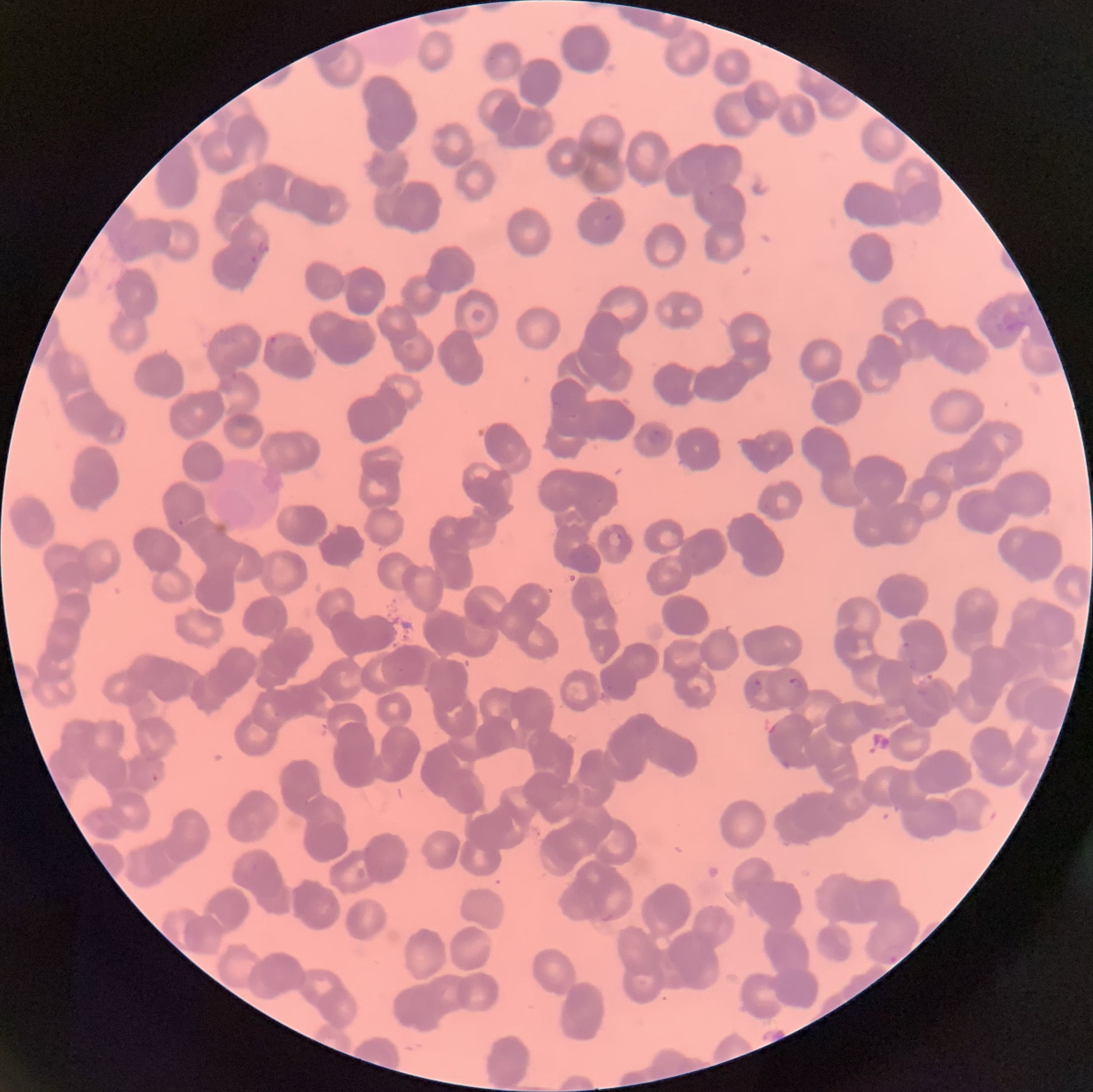
Summary:
  - Coordinate format: approximate bounding boxes as named x1/y1/x2/y2 corners in pixels
  - Plasmodium parasite locations: (x1=707, y1=190, x2=715, y2=196), (x1=604, y1=214, x2=615, y2=221), (x1=257, y1=237, x2=271, y2=254), (x1=250, y1=255, x2=259, y2=263), (x1=266, y1=335, x2=278, y2=347), (x1=552, y1=400, x2=562, y2=412), (x1=647, y1=429, x2=665, y2=444), (x1=607, y1=530, x2=623, y2=547), (x1=903, y1=641, x2=912, y2=649), (x1=909, y1=659, x2=917, y2=672), (x1=789, y1=676, x2=803, y2=689), (x1=754, y1=678, x2=762, y2=693), (x1=979, y1=795, x2=998, y2=831), (x1=882, y1=944, x2=901, y2=963)
  - Plasmodium parasites too small for a box (approximate object centers, named x/y in pixels): (x=181, y=522)
  - Preparation: thin blood film
  - Modality: light microscopy
  - Red blood cell morphology: rouleaux formation
  - Image size: 1093×1092 pixels